Outline platelets.
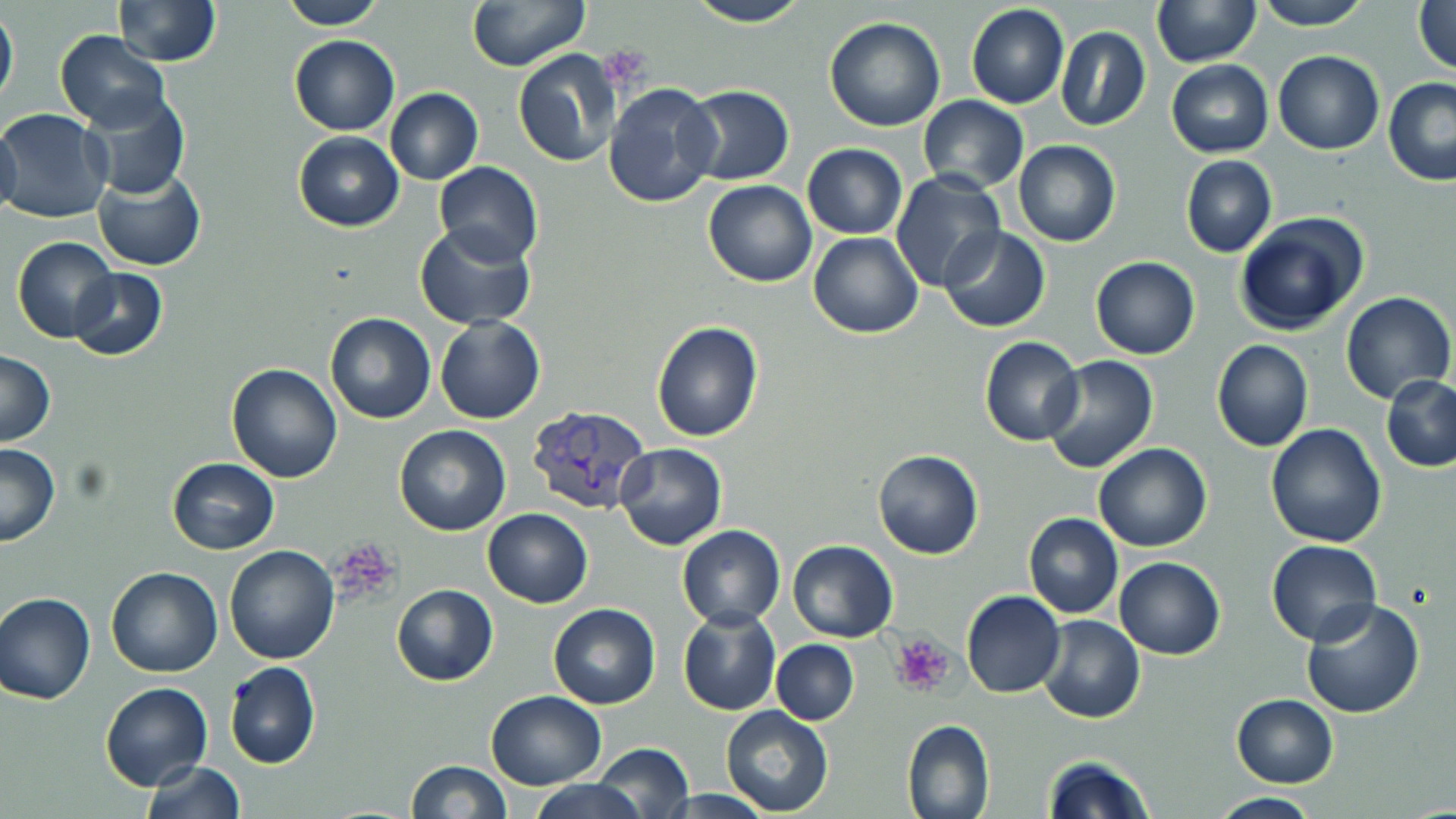

Approximate bounding boxes as (x1, y1, x2, y2) in pixels.
Platelets: (599, 42, 657, 96), (327, 542, 404, 610), (889, 632, 954, 694).

Uninfected red blood cell locations: (113, 0, 220, 66), (277, 0, 386, 30), (466, 0, 588, 71), (1152, 0, 1259, 67), (1413, 0, 1456, 77), (685, 1, 812, 27), (1253, 1, 1371, 29), (966, 5, 1068, 108), (0, 6, 18, 113), (824, 16, 945, 131), (1054, 25, 1150, 131), (56, 31, 170, 130), (289, 33, 400, 135), (513, 48, 622, 168), (1274, 50, 1384, 155), (1166, 60, 1274, 158), (1384, 76, 1456, 187), (603, 84, 721, 208), (682, 85, 794, 185), (80, 87, 191, 200), (384, 88, 482, 184), (919, 96, 1029, 193), (0, 109, 111, 225), (0, 121, 21, 220), (293, 130, 404, 232), (1013, 140, 1121, 248), (803, 144, 907, 237), (1181, 156, 1277, 258), (432, 160, 543, 266), (94, 168, 205, 272), (889, 170, 1008, 294), (703, 180, 816, 287), (1232, 213, 1368, 335), (413, 224, 538, 331), (939, 225, 1051, 332), (809, 232, 924, 338), (11, 236, 118, 343), (1091, 256, 1200, 360), (67, 268, 168, 361), (1339, 292, 1454, 405), (324, 313, 436, 424), (434, 316, 546, 424), (652, 320, 763, 441), (980, 336, 1084, 445), (1211, 340, 1313, 452), (0, 351, 56, 448), (1042, 356, 1158, 474), (227, 362, 343, 483), (1381, 374, 1456, 472), (1265, 423, 1388, 548), (393, 424, 511, 536), (0, 442, 60, 546), (614, 442, 728, 549), (1094, 442, 1213, 551), (873, 448, 984, 561), (168, 458, 278, 554), (483, 508, 594, 608), (1022, 512, 1124, 618), (676, 524, 785, 629), (788, 539, 898, 642), (1266, 540, 1381, 646), (223, 545, 341, 664), (1114, 556, 1224, 659), (105, 567, 224, 678), (392, 584, 497, 686), (962, 590, 1065, 699), (1, 593, 95, 705), (1299, 596, 1425, 718), (548, 603, 661, 709), (678, 607, 781, 716), (1037, 614, 1145, 722), (770, 638, 858, 725), (223, 660, 321, 770), (100, 682, 212, 791), (484, 689, 609, 790), (1232, 694, 1339, 787), (721, 706, 834, 815), (902, 719, 994, 819), (593, 744, 694, 818), (1042, 756, 1157, 819), (140, 760, 246, 818), (405, 760, 511, 818), (530, 779, 647, 819), (1208, 793, 1325, 818). Plasmodium vivax-infected red blood cell locations: (526, 401, 664, 517). Slide-level diagnosis: Plasmodium vivax. Image is 1456×819 pixels. May-Grünwald-Giemsa-stained preparation. One field of a larger specimen. Optical microscopy. Thin blood film. Captured at 1000x magnification.